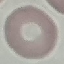 Malaria status: uninfected. Cell patch, automatically extracted from a larger field of view and resized to 64 × 64 pixels. Photographed with a smartphone camera at the microscope eyepiece. Thin blood film. Giemsa stain.